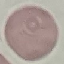
Summary:
  - Result: no malaria parasites detected
  - Stain: Giemsa
  - Capture: smartphone through the microscope eyepiece
  - Preparation: thin blood film
  - Image type: automatically extracted cell patch, resized to 64 × 64 pixels